Name the cell type shown.
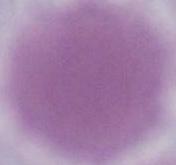

This is an erythrocyte.

{
  "modality": "photomicrograph",
  "magnification": "1000x"
}